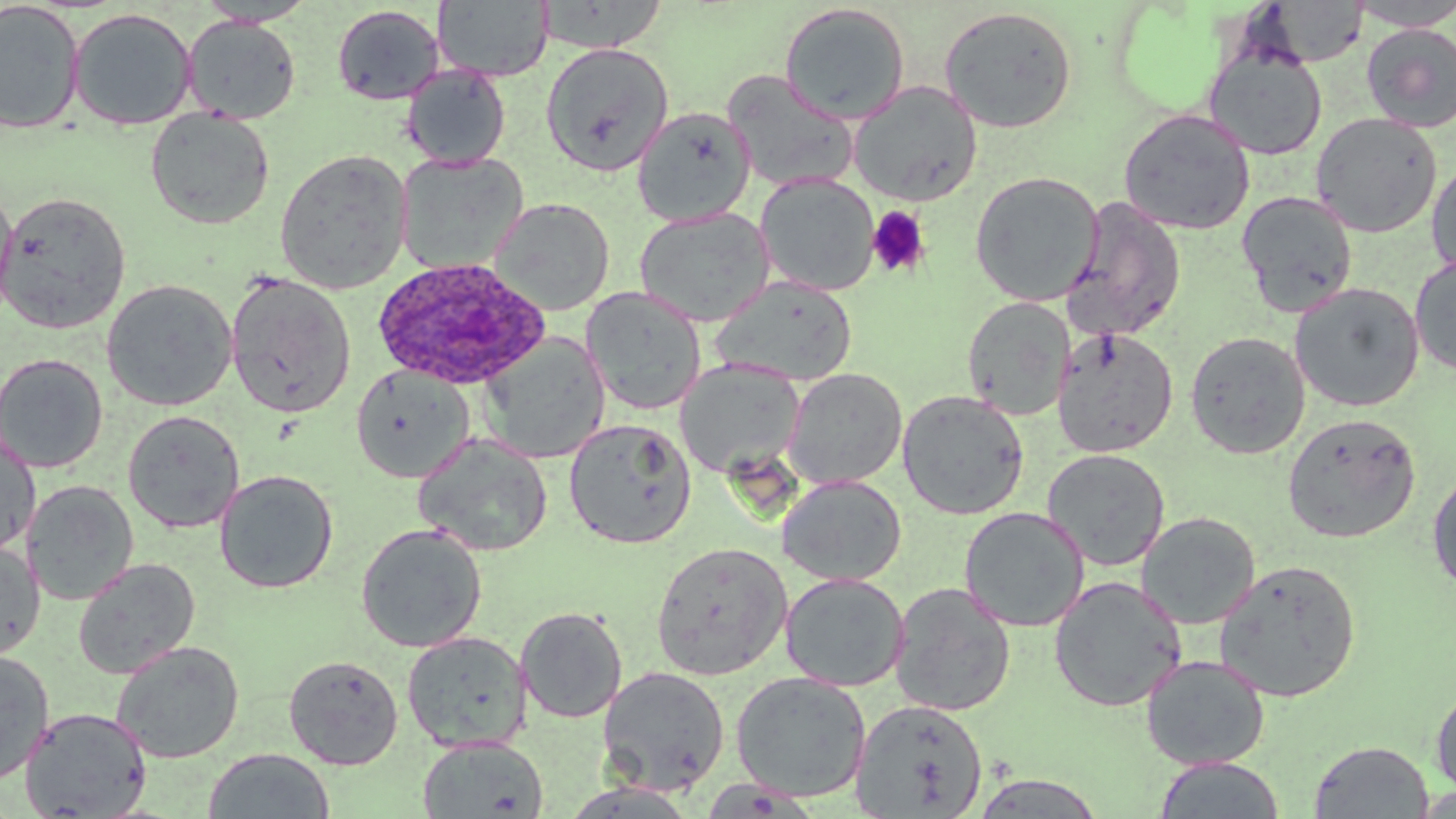
Approximate bounding boxes as (x1, y1, x2, y2) in pixels. Plasmodium ovale-infected red blood cell locations: (371, 256, 553, 391). Uninfected red blood cell locations: (433, 0, 553, 81), (196, 1, 316, 27), (1346, 1, 1456, 31), (1, 2, 85, 134), (1248, 2, 1370, 69), (778, 3, 910, 124), (331, 4, 445, 105), (938, 6, 1079, 134), (68, 8, 197, 130), (182, 16, 301, 124), (1360, 23, 1456, 133), (539, 42, 674, 176), (1204, 44, 1327, 161), (401, 66, 511, 169), (722, 70, 859, 193), (848, 80, 983, 206), (632, 106, 756, 226), (145, 108, 275, 230), (1118, 109, 1256, 235), (1310, 112, 1443, 237), (274, 149, 412, 294), (396, 152, 528, 274), (1427, 156, 1456, 278), (969, 171, 1104, 306), (755, 173, 879, 296), (0, 183, 18, 326), (1, 191, 132, 333), (1237, 191, 1359, 317), (489, 197, 615, 315), (1062, 197, 1187, 340), (634, 207, 775, 326), (1409, 255, 1456, 376), (225, 271, 357, 419), (712, 275, 858, 386), (101, 279, 238, 411), (1289, 281, 1425, 412), (581, 287, 706, 414), (961, 296, 1076, 420), (1052, 327, 1178, 458), (1185, 330, 1310, 458), (478, 333, 611, 463), (0, 352, 109, 473), (675, 360, 805, 478), (350, 364, 476, 483), (783, 368, 907, 488), (897, 389, 1030, 520), (122, 410, 245, 533), (1282, 412, 1422, 543), (563, 418, 697, 549), (0, 426, 40, 558), (414, 433, 553, 556), (1042, 448, 1170, 571), (1427, 466, 1456, 596), (214, 469, 339, 593), (777, 474, 906, 586), (24, 480, 139, 605), (958, 506, 1089, 631), (1136, 511, 1260, 629), (355, 524, 487, 652), (0, 540, 44, 660), (651, 541, 792, 681), (72, 558, 200, 680), (1214, 559, 1362, 702), (780, 572, 909, 692), (1049, 576, 1187, 712), (890, 582, 1017, 717), (515, 606, 628, 723), (402, 631, 530, 752), (110, 640, 245, 763), (0, 649, 55, 784), (283, 654, 403, 769), (1141, 654, 1270, 770), (598, 665, 730, 795), (730, 671, 871, 802), (1430, 680, 1456, 800), (850, 699, 988, 817), (19, 707, 152, 817), (417, 736, 548, 819), (1309, 740, 1434, 819), (202, 748, 335, 818), (1152, 757, 1287, 819), (968, 772, 1109, 817). Platelet locations: (866, 205, 932, 279). Slide-level diagnosis: Plasmodium ovale. May-Grünwald-Giemsa stain. Captured at 1000x magnification. Image is 1456×819 pixels. Optical microscopy. Thin blood film. Single field of view.